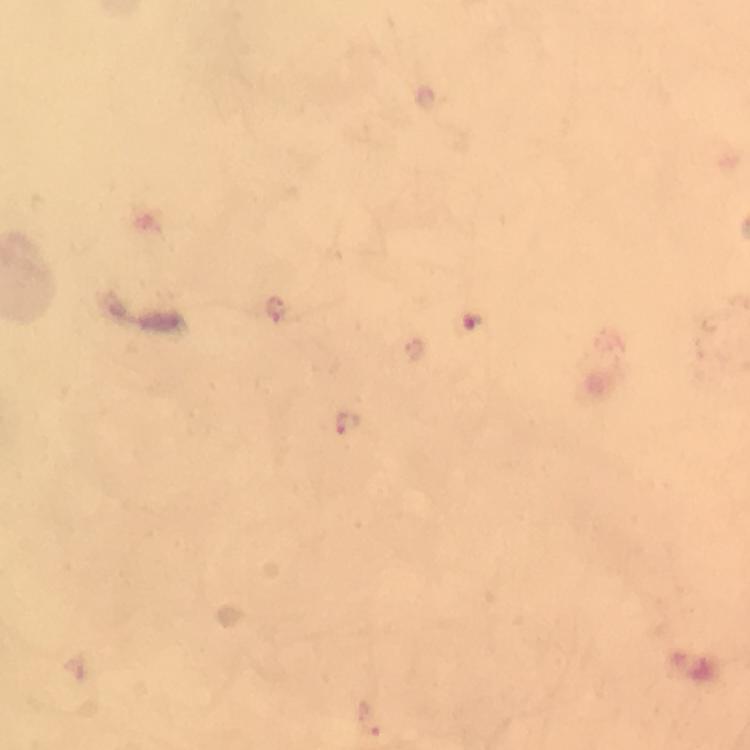
Approximate centers as {x, y} in pixels.
Summary:
  - Plasmodium parasite locations: {472, 321}, {350, 424}
  - Image size: 750×750 pixels
  - Immersion oil: applied
  - Preparation: thick blood smear
  - Magnification: 100x
  - Context: from a malaria diagnostic workup
  - Cropped from: one field of view
  - Capture: smartphone mounted on the microscope
  - Stain: Giemsa